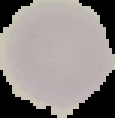

From a thin blood film. Segmented cell region on a black background. Image is 115×118 pixels. Result: no Plasmodium parasites seen.